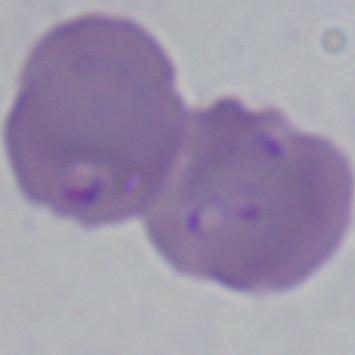

{
  "identification": "Babesia",
  "magnification": "1000x",
  "modality": "photomicrograph"
}